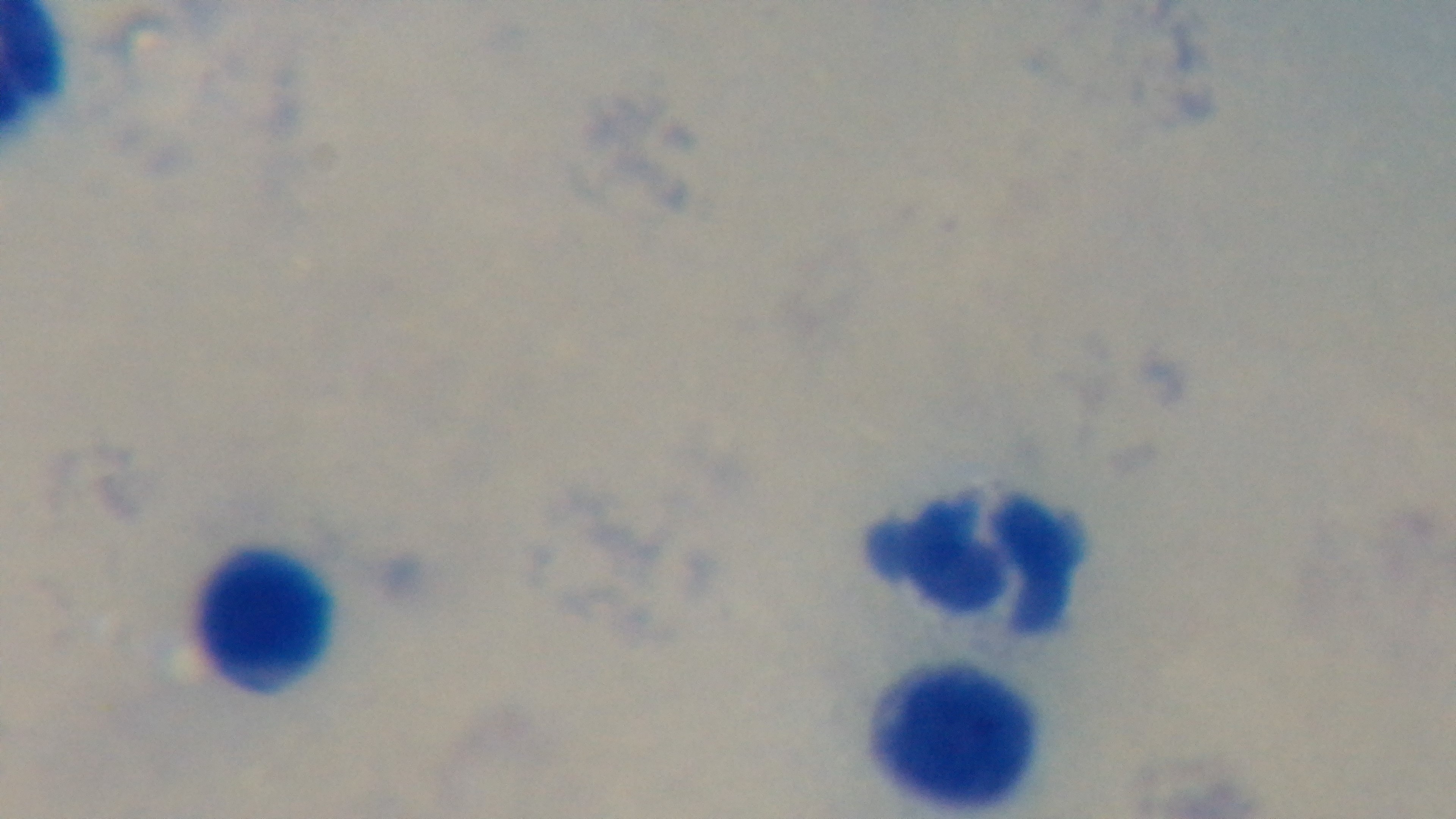
Summary:
  - Malaria status: uninfected
  - Preparation: thick blood film
  - Stain: Giemsa
  - Field of view: single
  - Modality: light microscopy
  - Capture: mounted 4K digital camera
  - Objective: 100x oil immersion